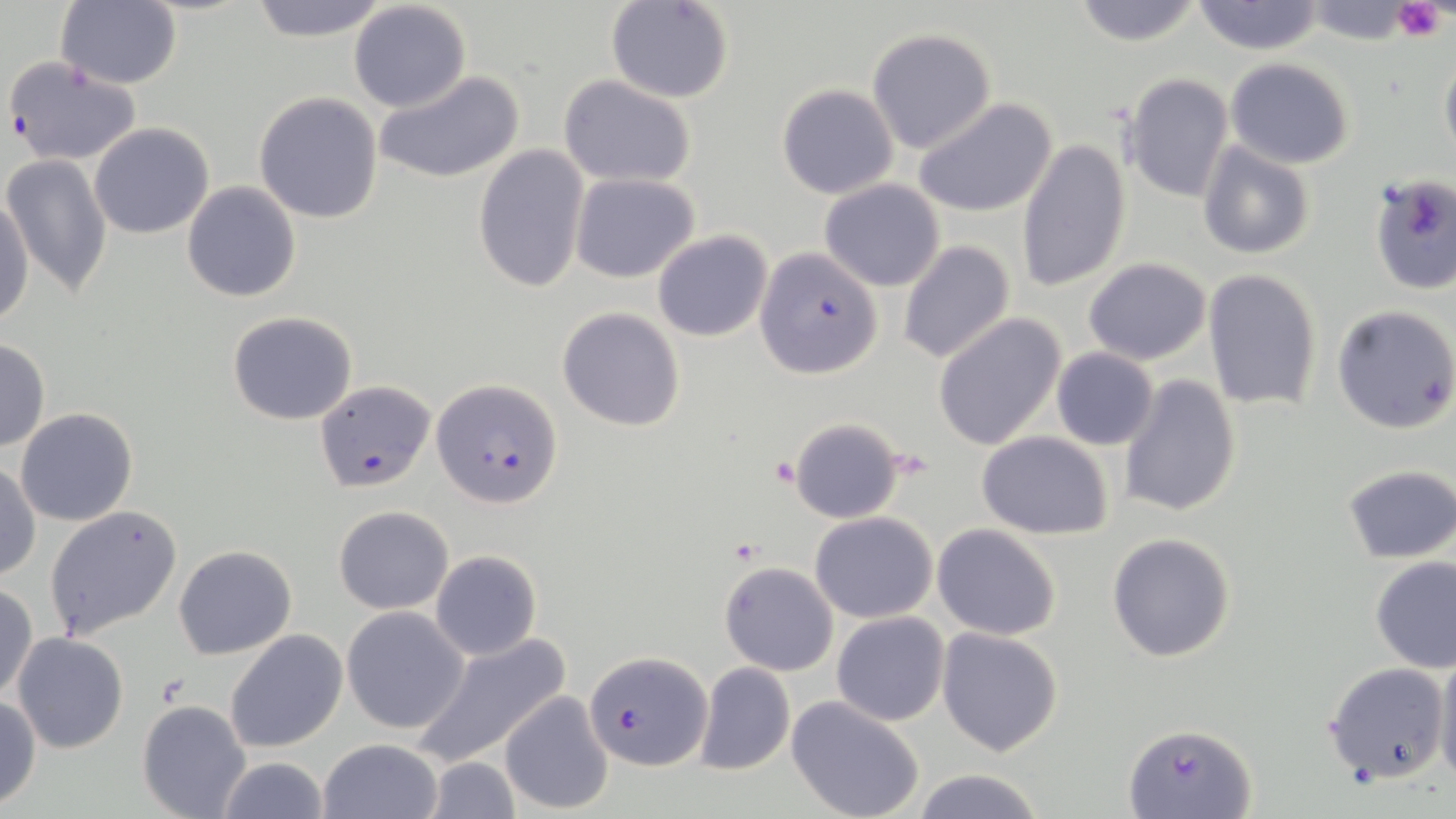 Approximate bounding boxes as (x1,y1)-(x2,y2) corner pairs in pixels. Uninfected red blood cell locations: (248,0)-(389,43), (1070,0)-(1206,47), (55,1)-(182,88), (348,1)-(471,114), (606,1)-(733,103), (1191,1)-(1325,55), (1299,1)-(1424,46), (867,28)-(997,154), (1439,44)-(1456,164), (1226,57)-(1353,168), (375,70)-(524,185), (1120,72)-(1234,204), (556,76)-(699,187), (777,83)-(900,199), (253,91)-(384,225), (913,97)-(1056,218), (89,123)-(215,239), (1016,138)-(1130,294), (1196,141)-(1316,260), (474,144)-(591,295), (2,154)-(113,299), (569,173)-(700,282), (1369,174)-(1456,296), (819,178)-(945,291), (181,182)-(302,302), (0,194)-(34,330), (652,230)-(773,342), (898,239)-(1015,366), (1083,258)-(1211,365), (1204,269)-(1322,413), (556,305)-(686,432), (1331,305)-(1456,435), (227,311)-(359,425), (934,312)-(1066,450), (0,339)-(50,452), (1051,348)-(1160,449), (1118,373)-(1242,518), (14,407)-(138,527), (787,416)-(908,524), (976,431)-(1114,538), (0,460)-(41,583), (1342,465)-(1456,563), (43,504)-(183,641), (333,504)-(455,614), (810,512)-(938,623), (931,524)-(1062,640), (1106,532)-(1237,663), (173,544)-(298,660), (429,549)-(542,661), (1369,557)-(1456,672), (719,561)-(838,676), (1,582)-(37,703), (341,606)-(471,734), (832,612)-(949,726), (937,627)-(1065,756), (225,629)-(347,753), (413,632)-(572,768), (12,633)-(128,754), (1434,645)-(1456,785), (1323,661)-(1448,786), (694,662)-(795,777), (499,692)-(614,812), (0,694)-(43,810), (787,696)-(925,819), (136,699)-(250,819), (319,738)-(444,819), (216,754)-(330,819), (423,756)-(522,819), (909,768)-(1046,819). Platelet locations: (1391,0)-(1447,44), (771,456)-(800,487), (726,538)-(761,565). Plasmodium falciparum-infected red blood cell locations: (3,54)-(143,167), (756,248)-(882,377), (434,379)-(563,507), (315,380)-(435,491), (585,650)-(710,771), (1124,721)-(1256,818). Slide-level diagnosis: Plasmodium falciparum. Thin blood smear. Optical microscopy. Captured at 1000x magnification. Image is 1456×819 pixels. One field of a larger specimen. May-Grünwald-Giemsa stain.